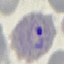
malaria status = parasitized
image type = automatically extracted cell patch, resized to 64 × 64 pixels
stain = Giemsa
capture = smartphone through the microscope eyepiece
preparation = thin smear